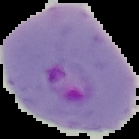

Cell region segmented out of the field of view; the surrounding area is masked to black. Result: malaria parasites identified. From a thin blood smear. Image is 139×139 pixels.